Outline each uninfected red blood cell.
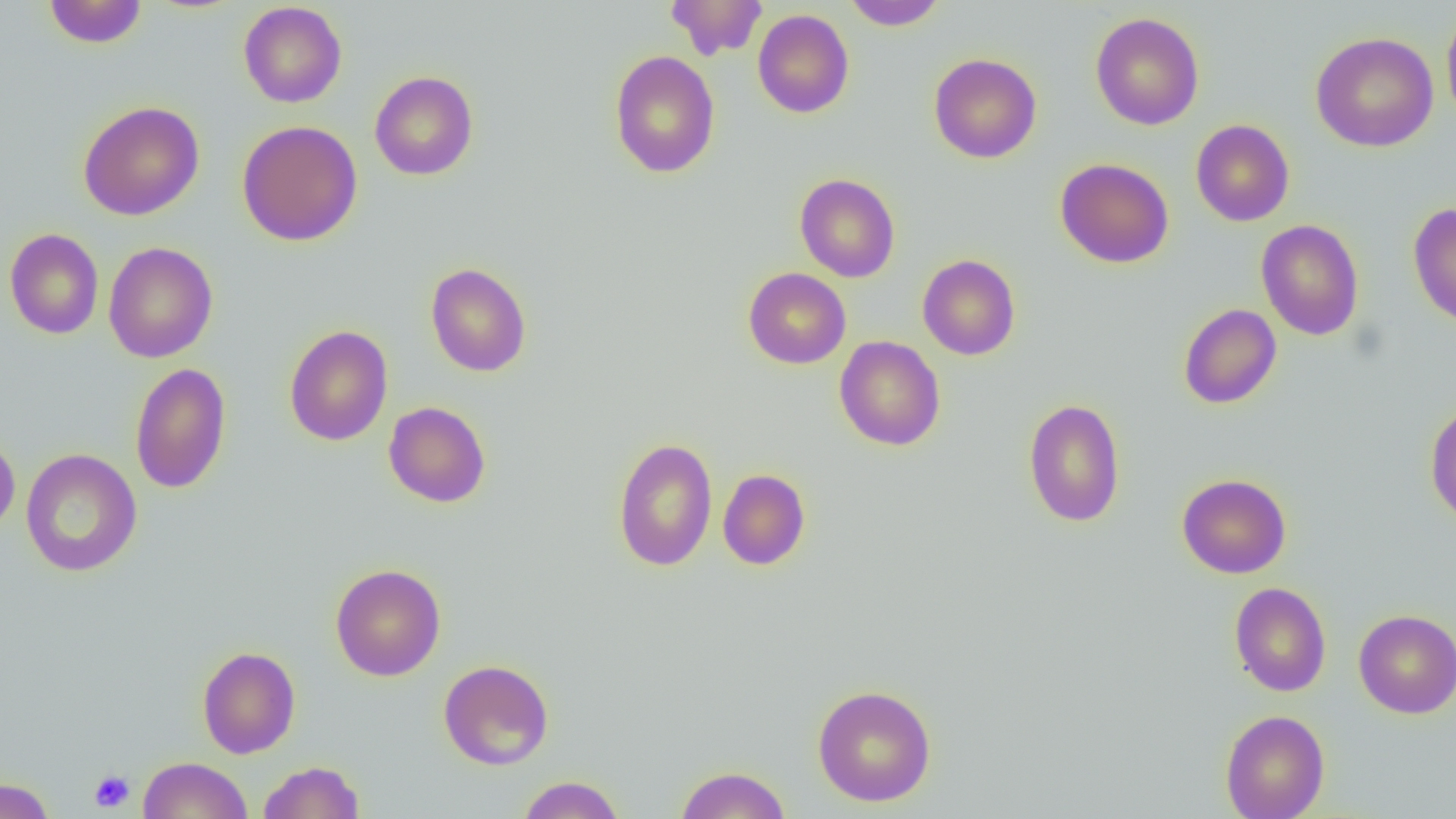
Approximate bounding boxes as (x1,y1)-(x2,y2) corner pairs in pixels.
Uninfected red blood cells: (44,0)-(147,48), (666,0)-(768,59), (843,0)-(948,29), (238,2)-(347,108), (1441,6)-(1456,129), (752,9)-(854,118), (1090,12)-(1204,131), (1310,31)-(1439,152), (608,50)-(721,178), (928,53)-(1042,163), (369,71)-(479,180), (78,101)-(205,221), (1190,119)-(1295,226), (237,120)-(363,246), (1055,158)-(1174,268), (795,174)-(901,282), (1407,202)-(1456,328), (1256,220)-(1365,340), (4,228)-(104,339), (122,239)-(222,492), (103,241)-(218,363), (917,254)-(1021,361), (425,262)-(531,377), (743,267)-(851,369), (1178,303)-(1282,409), (284,324)-(393,446), (834,336)-(946,451), (130,362)-(232,494), (1023,398)-(1126,528), (383,401)-(491,508), (1425,401)-(1456,526), (0,432)-(20,536), (612,437)-(718,572), (20,448)-(142,577), (717,468)-(811,570), (1177,473)-(1291,578), (330,563)-(446,681), (1229,582)-(1331,697), (1353,609)-(1456,718), (197,646)-(301,759), (438,659)-(554,770), (812,683)-(937,807), (1220,709)-(1330,819), (138,756)-(252,819), (257,760)-(365,818), (674,765)-(792,819), (517,775)-(625,818), (0,777)-(56,819).

Summary:
  - Platelet locations: (89,770)-(135,813)
  - Slide-level diagnosis: no evidence of blood parasites
  - Preparation: thin blood smear
  - Modality: optical microscopy
  - Field of view: one of a larger specimen
  - Image size: 1456×819 pixels
  - Magnification: 1000x